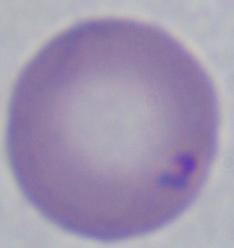

A Babesia parasite is seen. Captured at 1000x magnification. Micrograph.